Classify this cell by malaria status.
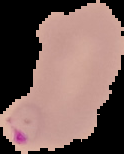

Parasitized.

From a thin blood film. The area outside the segmented cell region is set to black. Image is 124×154 pixels.